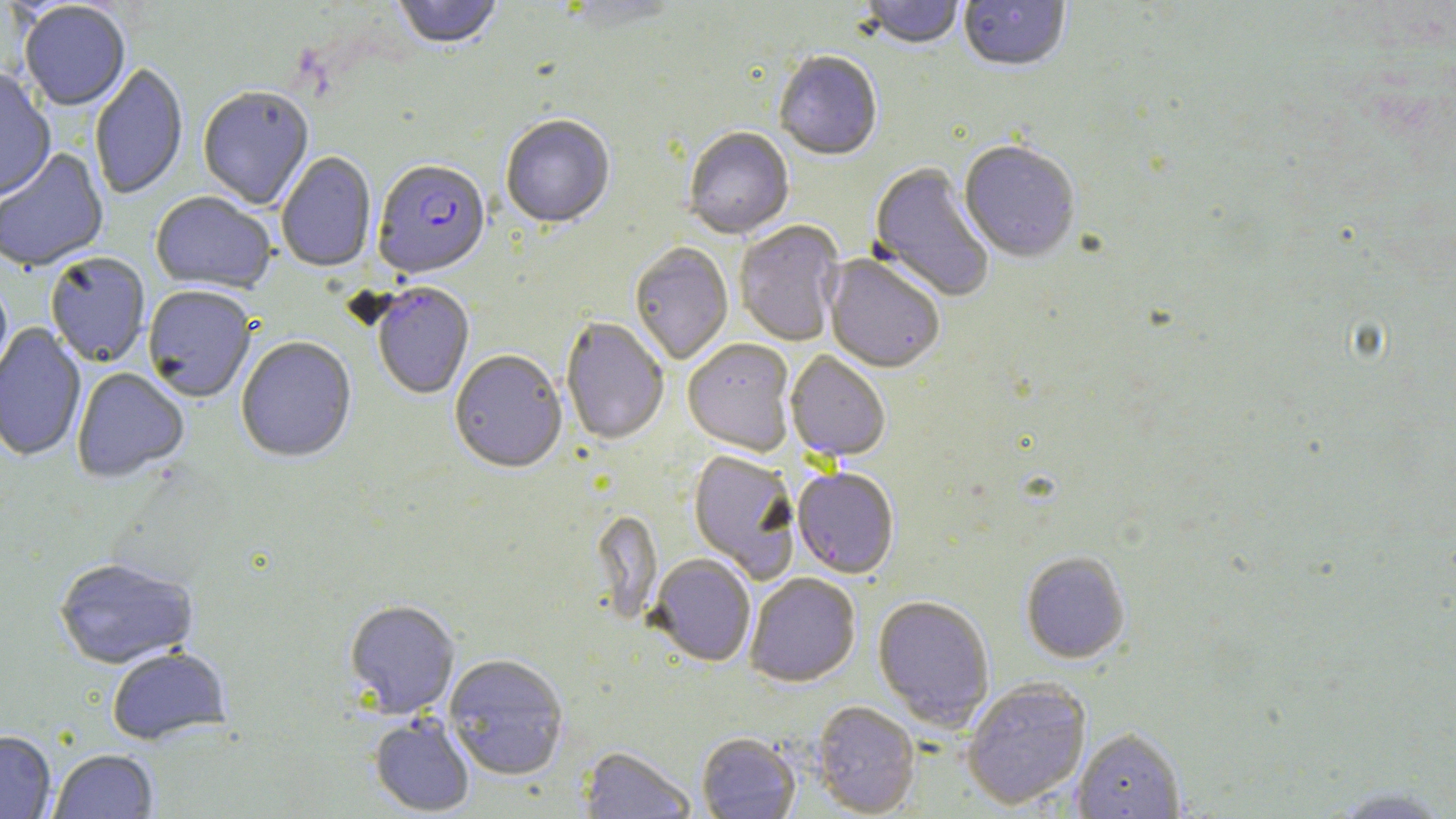

Summary:
  - Coordinate format: approximate bounding boxes as (x1,y1)-(x2,y2) corner pairs in pixels
  - Plasmodium falciparum-infected red blood cell locations: (372,162)-(491,281), (371,284)-(475,401)
  - Uninfected red blood cell locations: (392,0)-(504,53), (560,0)-(684,31), (860,0)-(965,52), (958,1)-(1071,75), (19,3)-(130,112), (774,53)-(883,163), (90,63)-(188,201), (0,70)-(56,202), (198,89)-(314,211), (500,116)-(615,231), (683,129)-(794,241), (958,143)-(1080,265), (0,149)-(109,274), (277,153)-(376,273), (868,164)-(994,303), (150,193)-(276,295), (734,221)-(846,346), (629,243)-(733,366), (46,254)-(150,368), (823,256)-(944,375), (0,283)-(14,391), (143,287)-(255,404), (561,318)-(669,446), (0,324)-(86,464), (237,338)-(357,464), (682,340)-(796,458), (785,351)-(890,462), (449,352)-(567,476), (72,369)-(189,484), (688,451)-(801,584), (792,469)-(899,579), (590,511)-(662,629), (1020,552)-(1131,665), (649,555)-(755,668), (54,559)-(198,671), (745,574)-(861,688), (873,596)-(994,731), (344,602)-(460,720), (106,649)-(232,746), (444,656)-(569,782), (962,679)-(1091,810), (811,702)-(920,816), (368,715)-(475,817), (1073,729)-(1185,818), (0,731)-(56,818), (696,734)-(800,819), (578,746)-(696,818), (50,750)-(158,818), (1323,785)-(1456,818)
  - Slide-level diagnosis: Plasmodium falciparum
  - Stain: May-Grünwald-Giemsa
  - Preparation: thin blood film
  - Field of view: one of a larger specimen
  - Image size: 1456×819 pixels
  - Magnification: 1000x
  - Modality: light microscopy